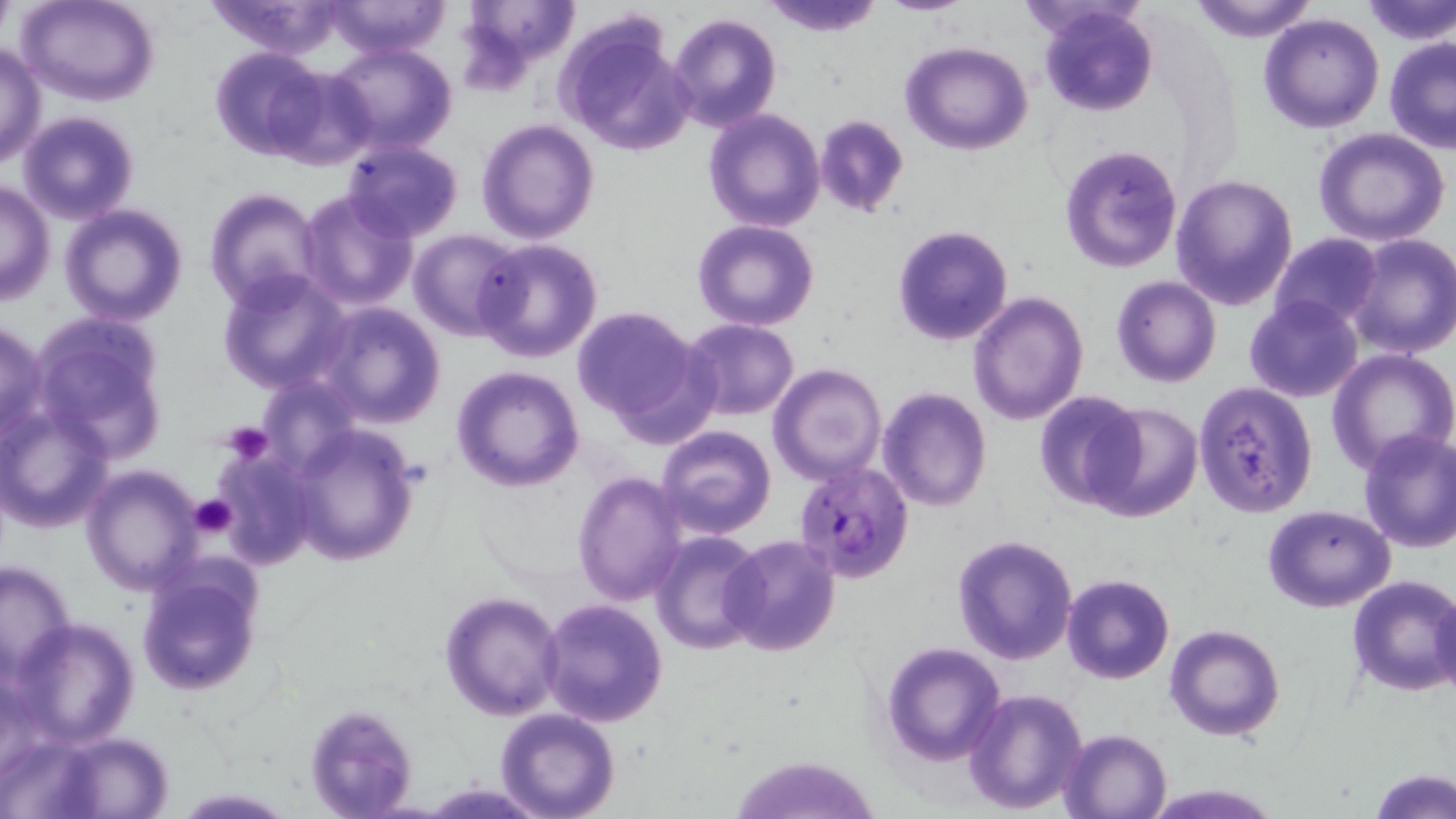

Approximate bounding boxes as (x1,y1)-(x2,y2) corner pairs in pixels. Plasmodium falciparum-infected red blood cell locations: (779,465)-(911,580). Uninfected red blood cell locations: (19,0)-(159,106), (203,0)-(350,60), (325,0)-(452,58), (455,0)-(579,86), (761,0)-(886,37), (874,0)-(975,16), (1188,0)-(1324,43), (1356,0)-(1455,43), (1039,4)-(1158,116), (666,13)-(781,133), (1258,13)-(1384,133), (556,17)-(694,157), (1383,36)-(1456,152), (326,40)-(457,152), (901,41)-(1032,154), (0,42)-(46,168), (210,46)-(331,161), (702,108)-(827,232), (17,110)-(140,225), (812,113)-(910,218), (476,119)-(599,243), (1312,128)-(1452,245), (343,141)-(464,241), (1060,142)-(1185,272), (1169,171)-(1297,308), (0,179)-(55,306), (203,189)-(326,311), (298,190)-(420,312), (59,202)-(189,326), (691,219)-(820,331), (891,225)-(1014,347), (409,230)-(525,340), (1270,232)-(1383,331), (1342,233)-(1456,357), (473,238)-(604,364), (217,268)-(351,394), (1111,276)-(1222,388), (967,292)-(1089,426), (1243,295)-(1364,404), (315,301)-(447,427), (571,305)-(711,437), (30,315)-(169,461), (680,318)-(801,420), (0,320)-(48,442), (1328,349)-(1456,475), (769,362)-(887,484), (451,366)-(585,493), (1194,381)-(1318,518), (877,387)-(993,513), (1032,391)-(1145,511), (1085,400)-(1204,524), (1,403)-(117,532), (288,425)-(417,565), (656,425)-(776,540), (1356,428)-(1456,553), (213,445)-(320,569), (81,465)-(204,595), (571,470)-(688,605), (1262,504)-(1396,612), (651,530)-(765,655), (721,534)-(843,657), (950,534)-(1078,666), (0,560)-(78,679), (137,565)-(262,695), (1062,573)-(1176,684), (1347,574)-(1456,697), (1429,590)-(1456,697), (439,591)-(565,720), (539,599)-(668,726), (12,618)-(140,747), (1164,623)-(1285,740), (880,641)-(1007,767), (963,687)-(1089,814), (301,705)-(418,818), (494,709)-(620,819), (1059,728)-(1171,819), (53,733)-(176,818), (729,750)-(878,819), (1371,769)-(1454,819), (422,781)-(546,817), (169,787)-(297,817). Platelet locations: (219,419)-(272,464), (188,494)-(237,539). Slide-level diagnosis: Plasmodium falciparum. Thin blood smear. May-Grünwald-Giemsa stain. Image is 1456×819 pixels. Single field of view. Captured at 1000x magnification. Light microscopy.